Report the malaria status of this cell.
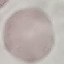
It is uninfected.

Photographed with a smartphone camera at the microscope eyepiece. Giemsa-stained preparation. Thin smear of blood. Cell patch, automatically extracted from a larger field of view and resized to 64 × 64 pixels.